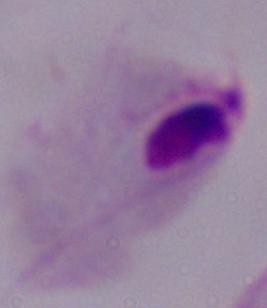

magnification = 1000x
identification = trichomonad
modality = micrograph